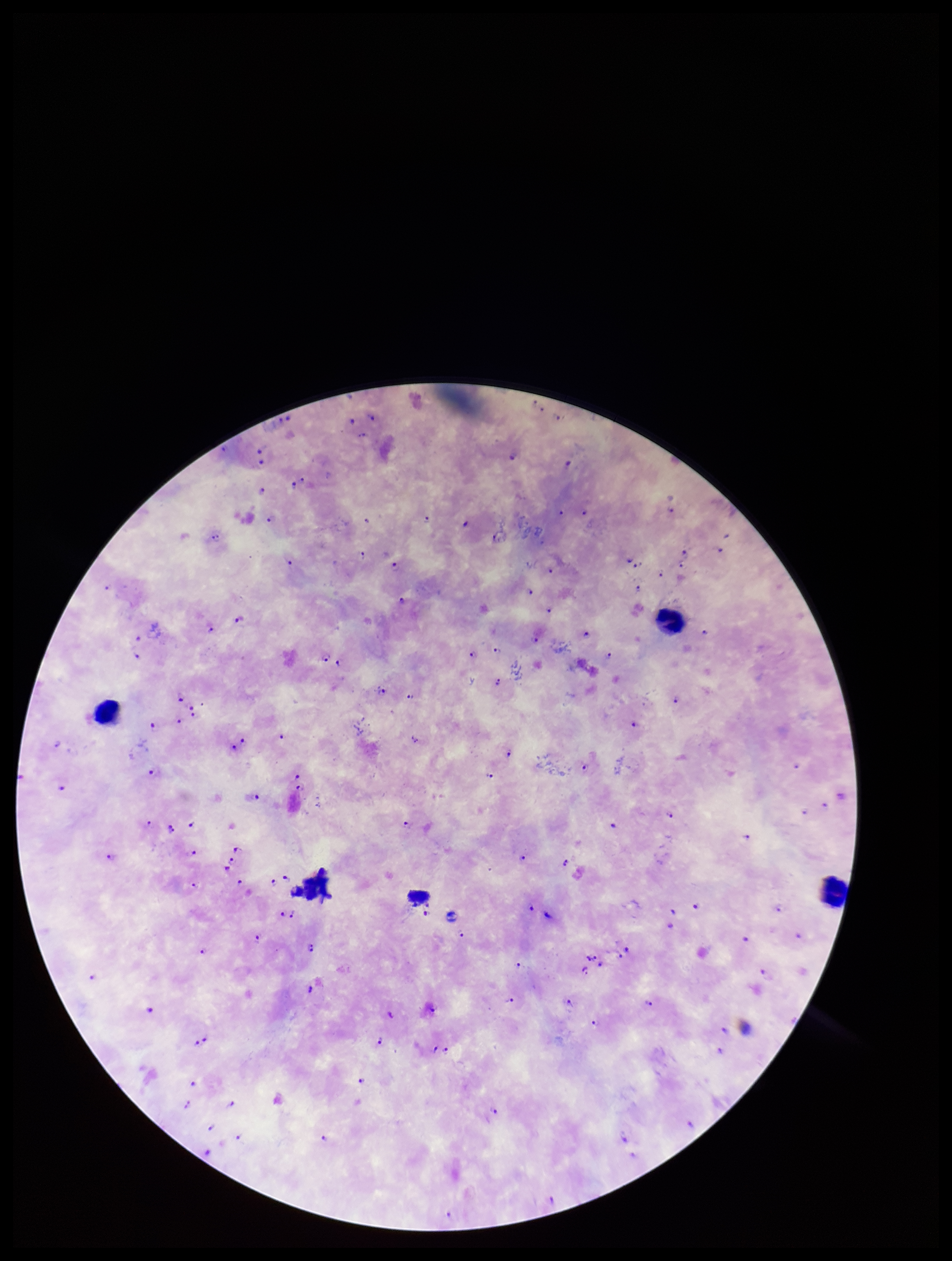
leukocyte_count: 4
capture: smartphone photograph through the microscope eyepiece
parasite_count: 105
preparation: thick smear
species_reported_for_this_patient: Plasmodium falciparum
field_of_view: single
stain: Giemsa
image_size: 952×1261 pixels
plasmodium_parasites: identified
patient_malaria_status: positive